Classify this cell by malaria status.
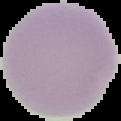
It is uninfected.

Segmented cell region on a black background. Image is 121×121 pixels. From a thin blood smear.